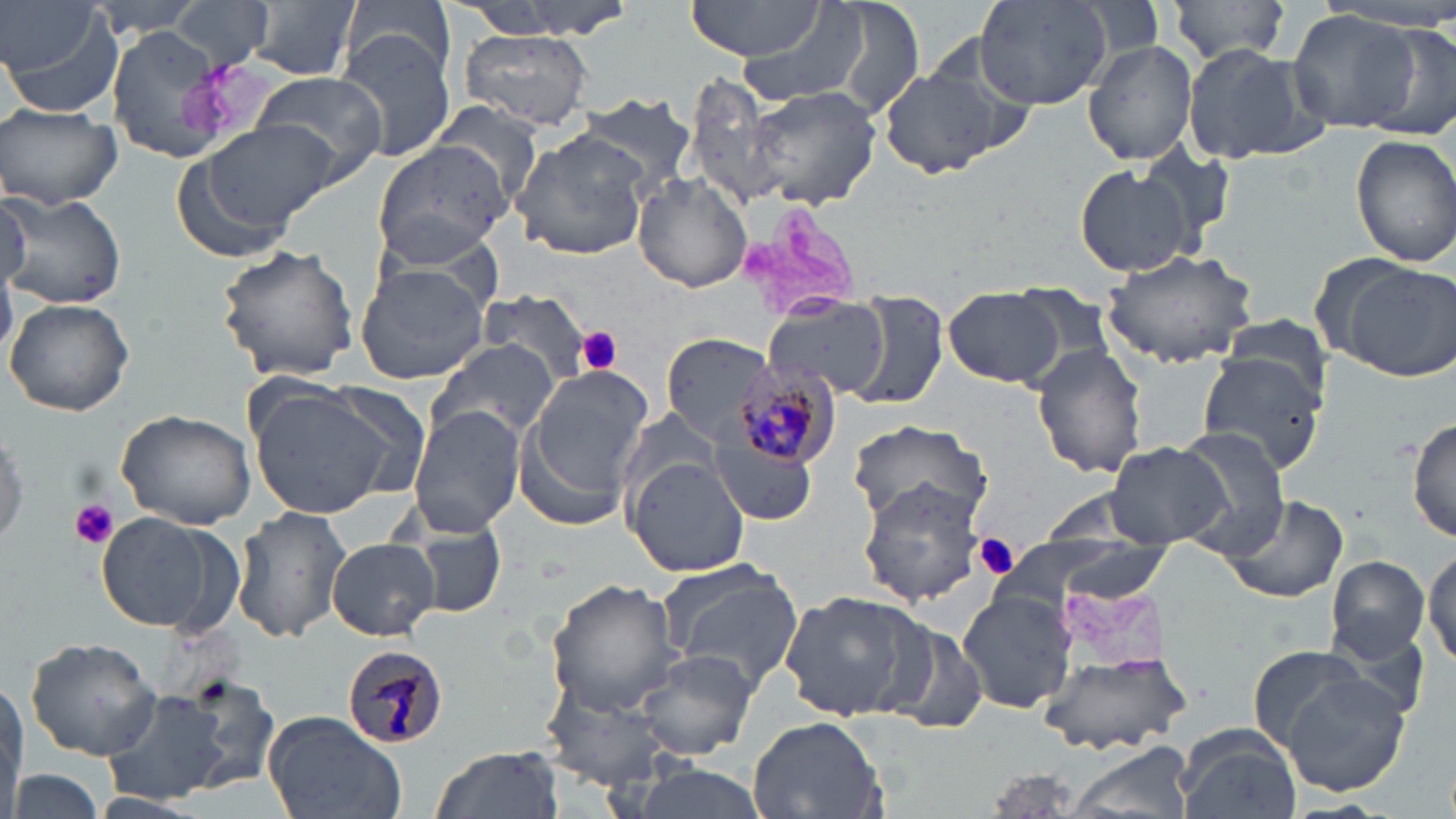
Approximate bounding boxes as (x1,y1)-(x2,y2) corner pairs in pixels. Uninfected red blood cell locations: (85,0)-(208,37), (172,0)-(274,72), (245,0)-(361,81), (453,0)-(627,36), (684,0)-(828,61), (819,0)-(926,121), (973,0)-(1112,109), (1167,0)-(1292,64), (739,1)-(871,107), (344,2)-(459,80), (2,5)-(124,116), (1289,11)-(1420,135), (1369,21)-(1456,137), (102,22)-(233,165), (335,28)-(455,161), (459,28)-(596,131), (1083,40)-(1199,166), (1182,43)-(1326,166), (879,66)-(1002,179), (249,68)-(393,186), (684,74)-(787,214), (743,83)-(883,211), (573,94)-(697,196), (432,101)-(548,208), (0,104)-(123,210), (198,119)-(336,232), (509,130)-(651,261), (1351,132)-(1456,268), (370,138)-(513,265), (1134,142)-(1234,250), (169,151)-(301,265), (1076,165)-(1192,277), (633,173)-(753,293), (1,187)-(127,311), (215,243)-(360,381), (1102,247)-(1262,367), (1335,258)-(1456,381), (354,260)-(490,386), (941,289)-(1065,387), (475,292)-(594,384), (842,293)-(952,411), (5,297)-(134,418), (764,298)-(889,399), (660,333)-(776,446), (427,339)-(558,444), (1033,342)-(1149,479), (1196,350)-(1326,477), (526,366)-(655,504), (248,383)-(403,520), (408,405)-(524,536), (117,410)-(256,532), (1407,415)-(1456,547), (846,418)-(990,528), (0,419)-(28,554), (1170,426)-(1290,558), (711,433)-(814,524), (1103,443)-(1232,549), (623,455)-(749,576), (857,480)-(991,606), (1216,494)-(1349,605), (232,506)-(352,644), (392,506)-(507,621), (96,513)-(234,633), (992,532)-(1175,615), (328,539)-(440,640), (1424,540)-(1456,671), (1325,553)-(1431,664), (655,557)-(805,689), (544,579)-(680,713), (956,588)-(1078,714), (778,591)-(924,722), (880,618)-(992,734), (24,637)-(161,760), (1245,646)-(1372,750), (631,648)-(759,759), (1039,651)-(1188,757), (1272,671)-(1413,799), (539,672)-(687,791), (175,677)-(282,793), (102,688)-(233,804), (263,711)-(407,819), (746,715)-(889,819), (1175,724)-(1302,819), (1065,744)-(1197,819), (430,746)-(564,819), (630,765)-(769,819), (6,768)-(108,819). Plasmodium malariae-infected red blood cell locations: (730,361)-(842,472), (341,642)-(449,751). Platelet locations: (577,327)-(624,375), (66,497)-(121,550), (973,535)-(1021,582). Slide-level diagnosis: Plasmodium malariae. Light microscopy. 1000x magnification. Image is 1456×819 pixels. Thin blood film. One field of a larger specimen. May-Grünwald-Giemsa-stained preparation.